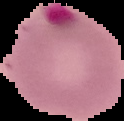 Result: malaria parasites detected. Segmented cell region on a black background. From a thin blood film. Image is 124×121 pixels.